Look for Plasmodium parasites.
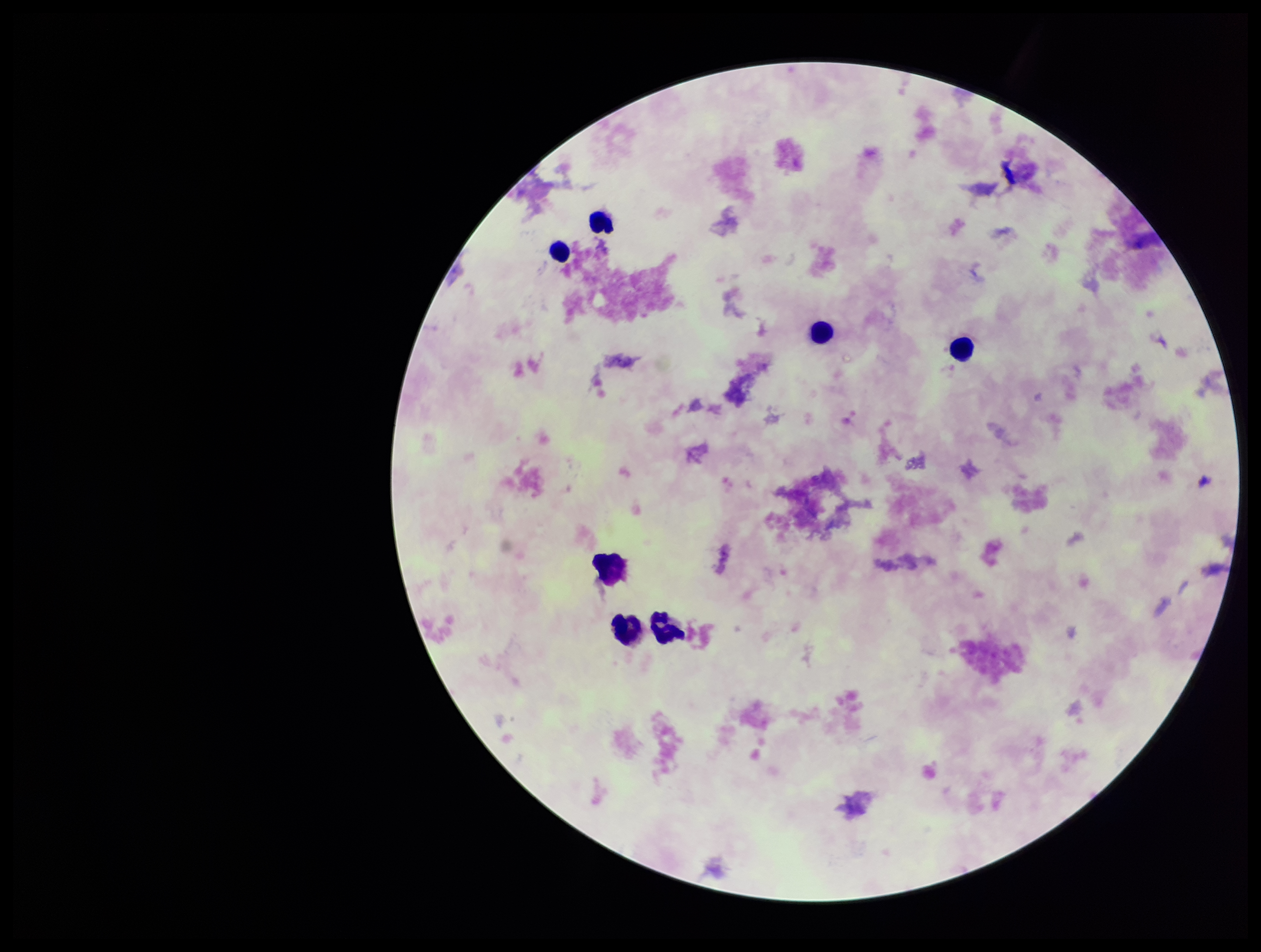
None detected.

patient malaria status = negative
capture = smartphone photograph through the microscope eyepiece
leukocyte count = 7
stain = Giemsa
parasite count = 0
image size = 1261×952 pixels
field of view = one from this slide
preparation = thick